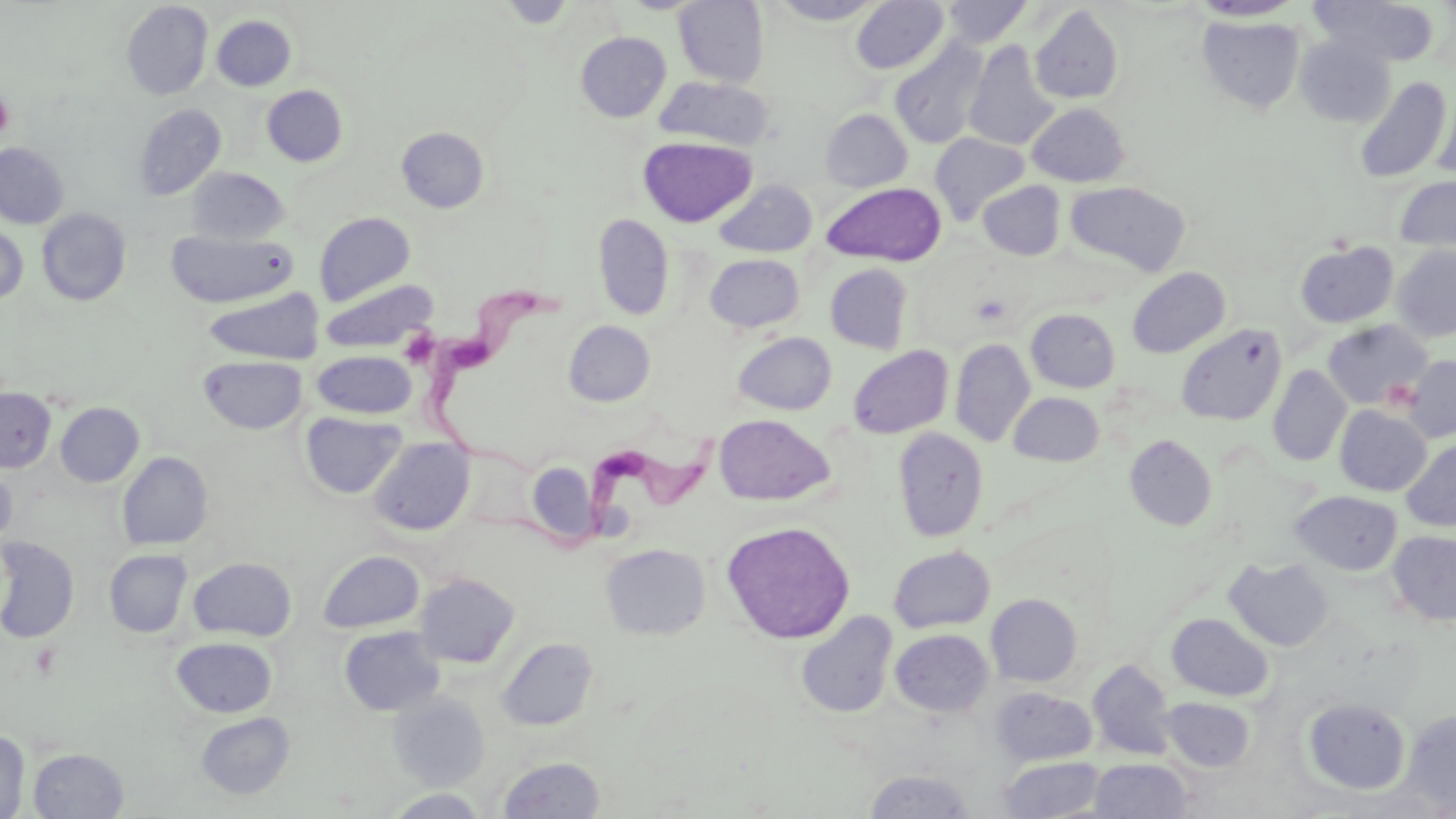

Summary:
  - Coordinate format: approximate bounding boxes as (x1, y1, x2, y2) in pixels
  - Uninfected red blood cell locations: (496, 0, 577, 28), (674, 0, 770, 87), (768, 0, 886, 25), (851, 0, 949, 74), (1310, 0, 1440, 67), (121, 1, 213, 100), (942, 1, 1033, 47), (1189, 1, 1304, 22), (1030, 4, 1124, 105), (211, 15, 296, 91), (1197, 15, 1305, 114), (576, 31, 671, 122), (1294, 34, 1396, 128), (890, 38, 989, 149), (964, 41, 1060, 151), (655, 76, 775, 151), (1353, 76, 1452, 183), (262, 85, 348, 166), (1432, 95, 1456, 181), (1027, 103, 1130, 186), (134, 104, 226, 200), (821, 109, 912, 191), (396, 126, 489, 213), (930, 133, 1029, 224), (638, 136, 757, 227), (0, 142, 69, 228), (186, 167, 289, 244), (1395, 175, 1456, 255), (714, 180, 817, 257), (978, 181, 1066, 260), (1065, 181, 1191, 276), (822, 182, 946, 266), (37, 208, 131, 305), (314, 212, 415, 306), (593, 214, 674, 320), (0, 225, 28, 304), (167, 230, 297, 308), (1295, 241, 1399, 328), (1393, 245, 1456, 342), (705, 253, 805, 332), (825, 264, 913, 353), (1127, 267, 1230, 358), (320, 278, 437, 353), (203, 289, 325, 364), (1026, 309, 1120, 392), (565, 320, 655, 406), (1323, 320, 1432, 409), (1177, 323, 1286, 425), (733, 332, 836, 415), (950, 338, 1035, 447), (848, 345, 953, 439), (312, 350, 417, 418), (199, 355, 308, 434), (1401, 355, 1456, 442), (1267, 365, 1351, 467), (0, 388, 56, 472), (1009, 391, 1104, 466), (56, 403, 144, 487), (1335, 405, 1432, 496), (300, 411, 406, 499), (714, 414, 835, 506), (893, 427, 988, 542), (1125, 434, 1217, 531), (369, 437, 475, 535), (1401, 438, 1456, 532), (117, 451, 213, 550), (527, 461, 599, 545), (0, 464, 16, 550), (1290, 491, 1402, 576), (721, 520, 855, 643), (1387, 530, 1456, 626), (0, 538, 79, 643), (601, 544, 710, 639), (889, 546, 995, 633), (104, 549, 192, 638), (318, 550, 424, 633), (188, 557, 296, 641), (1224, 557, 1335, 651), (414, 572, 520, 668), (986, 594, 1082, 686), (796, 611, 897, 718), (1166, 613, 1273, 701), (339, 626, 445, 716), (890, 629, 994, 717), (172, 637, 277, 717), (497, 637, 598, 731), (1088, 660, 1176, 760), (991, 687, 1097, 766), (389, 693, 490, 788), (1160, 696, 1255, 772), (1303, 697, 1411, 794), (1401, 710, 1456, 813), (195, 712, 296, 800), (0, 730, 30, 819), (28, 747, 128, 818), (498, 756, 605, 818), (999, 756, 1106, 817), (1089, 758, 1192, 818), (864, 769, 975, 818), (382, 789, 491, 818)
  - Trypanosoma brucei locations: (417, 281, 563, 478), (473, 427, 725, 554)
  - Platelet locations: (0, 91, 15, 140), (399, 327, 440, 367)
  - Slide-level diagnosis: Trypanosoma brucei
  - Field of view: single
  - Image size: 1456×819 pixels
  - Preparation: thin blood film
  - Modality: optical microscopy
  - Magnification: 1000x
  - Stain: May-Grünwald-Giemsa